Locate every parasitized red blood cell.
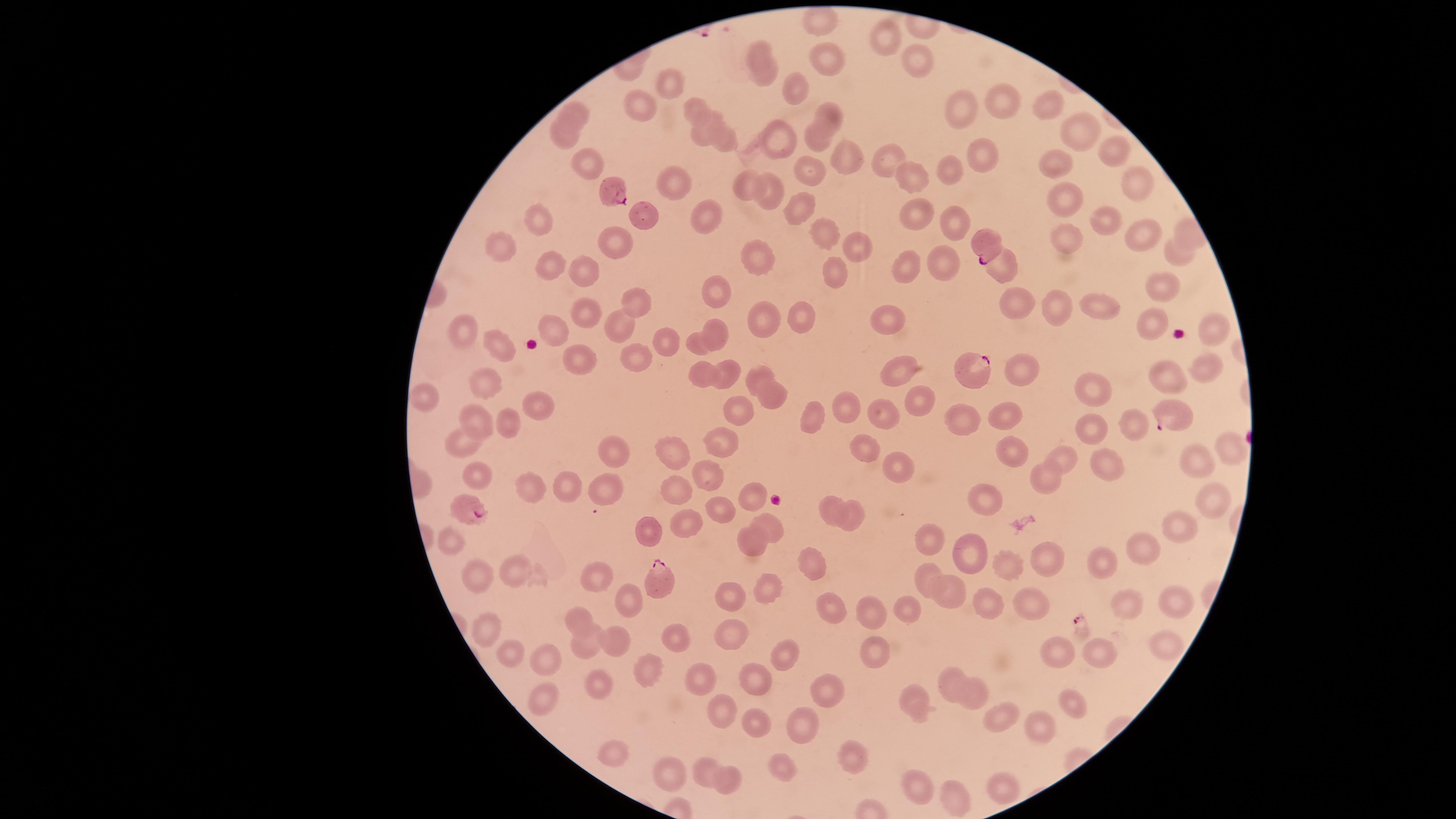

Approximate marker points as (x, y) in pixels.
Parasitized red blood cells: (616, 193), (987, 246), (970, 372), (1169, 415), (464, 506), (660, 582).

Approximate marker points as (x, y) in pixels. Uninfected red blood cells: (818, 20), (885, 34), (755, 48), (832, 63), (916, 64), (763, 76), (669, 81), (797, 89), (1000, 96), (694, 105), (1052, 105), (640, 109), (830, 110), (965, 110), (579, 111), (704, 126), (1079, 127), (557, 134), (781, 134), (816, 137), (728, 140), (981, 148), (1112, 150), (844, 159), (891, 160), (585, 163), (1053, 165), (959, 170), (809, 171), (905, 176), (746, 180), (673, 182), (1135, 182), (1063, 196), (768, 199), (801, 206), (912, 208), (706, 211), (542, 215), (644, 217), (1101, 218), (956, 219), (824, 234), (1135, 234), (1067, 237), (857, 244), (504, 245), (614, 246), (1176, 251), (755, 258), (941, 262), (548, 267), (907, 267), (999, 270), (584, 272), (834, 273), (1163, 287), (713, 293), (643, 303), (582, 307), (1021, 307), (1104, 307), (1063, 310), (760, 313), (891, 319), (618, 323), (797, 324), (1150, 324), (466, 327), (556, 328), (1214, 329), (718, 332), (665, 334), (693, 341), (498, 346), (640, 358), (575, 360), (1208, 363), (902, 368), (732, 373), (1025, 374), (694, 375), (760, 377), (1174, 378), (1094, 382), (493, 383), (770, 396), (921, 396), (426, 404), (537, 408), (842, 410), (741, 411), (878, 414), (481, 416), (815, 417), (965, 418), (1006, 418), (1127, 418), (510, 426), (1092, 431), (718, 435), (463, 444), (619, 444), (864, 444), (1232, 447), (1012, 451), (676, 454), (1064, 456), (1202, 460), (1106, 465), (898, 468), (704, 470), (482, 473), (1044, 474), (531, 483), (600, 484), (571, 487), (676, 488), (757, 498), (1205, 501), (990, 502), (828, 507), (723, 510), (855, 516), (690, 522), (766, 525), (1181, 526), (655, 537), (753, 538), (454, 542), (933, 542), (972, 553), (1146, 553), (1046, 562), (1106, 563), (1012, 564), (815, 565), (515, 568), (925, 572), (589, 574), (475, 577), (767, 592), (956, 598), (627, 601), (731, 601), (1125, 602), (1173, 604), (1028, 605), (832, 606), (990, 607), (863, 609), (908, 609), (579, 611), (489, 628), (733, 637), (1165, 637), (672, 638), (582, 639), (613, 639), (878, 649), (498, 651), (1106, 652), (784, 653), (1062, 656), (545, 660), (642, 670), (704, 674), (949, 678), (757, 679), (595, 683), (826, 693), (912, 696), (969, 696), (545, 703), (1070, 703), (717, 704), (761, 715), (1004, 721), (793, 724), (1037, 733), (610, 751), (854, 756), (702, 767), (785, 767), (731, 775), (665, 777), (1002, 783), (916, 785), (954, 800). Photographed with a smartphone camera through the microscope eyepiece. Giemsa-stained preparation. Species: Plasmodium falciparum. One field of view of the specimen. Thin blood smear. Image is 1456×819 pixels. The visible region is circular.